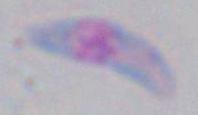

identification = Toxoplasma gondii
modality = micrograph
magnification = 1000x